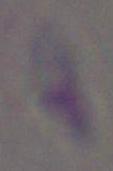

identification = Toxoplasma gondii
modality = micrograph
magnification = 1000x